Locate every leukocyte (white blood cell).
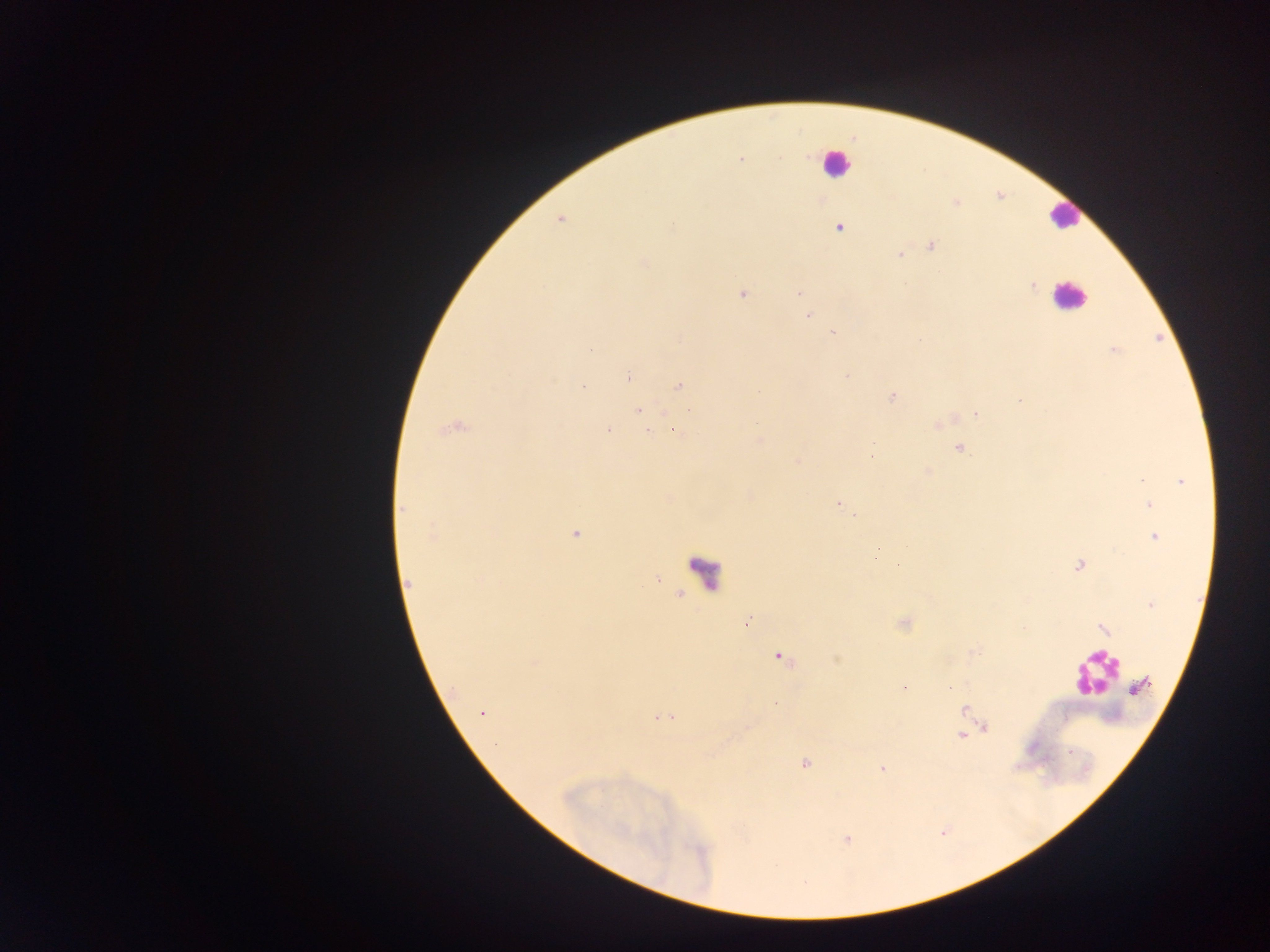
Approximate centers as x y in pixels.
Leukocytes: 836 162; 1063 216; 1068 296; 705 572; 1093 674.

{
  "malaria_parasite_locations": "approximate centers as x y in pixels: 779 158; 740 160; 559 219; 673 224; 839 228; 932 245; 899 255; 644 263; 1033 286; 799 293; 743 295; 809 316; 833 332; 590 349; 1114 350; 847 376; 629 378; 678 386; 583 387; 892 397; 638 410; 690 410; 977 413; 756 422; 644 423; 453 429; 608 429; 647 431; 675 431; 873 443; 959 448; 871 458; 796 461; 928 471; 1181 481; 1141 482; 837 504; 1150 505; 402 508; 855 515; 574 533; 432 535; 1155 537; 875 558; 1078 565; 408 583; 1150 605; 747 622; 1104 629; 779 657; 1142 686; 903 688; 775 703; 963 709; 482 714; 663 718; 983 728; 962 735; 805 763; 882 768",
  "image_size": "1270×952 pixels",
  "country": "Ghana",
  "capture": "mobile-phone photograph through a microscope",
  "preparation": "thick blood film",
  "field_of_view": "single"
}